Comment on the morphology of the red blood cells.
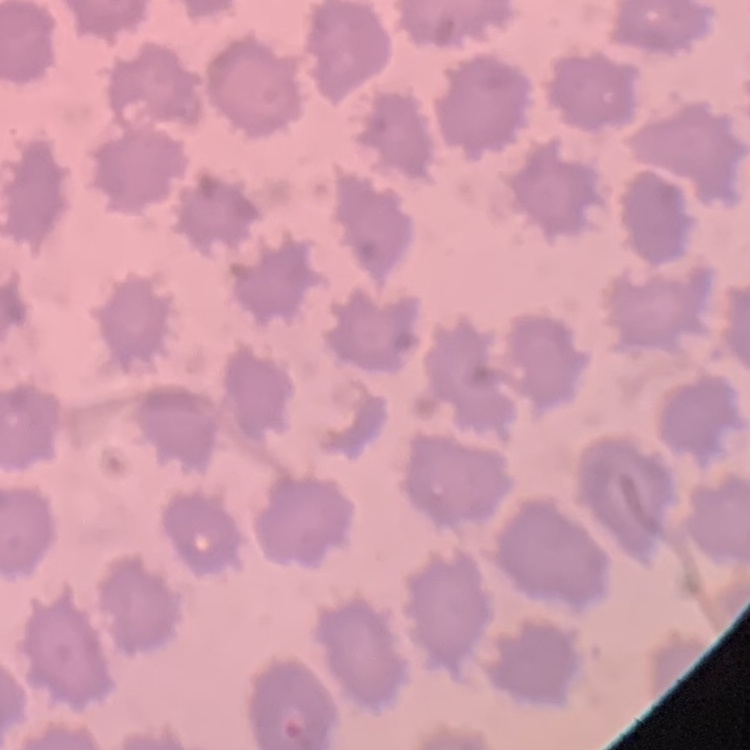
No rouleaux formation.

Field's or Giemsa stain. Thin blood smear. Square crop of a larger photomicrograph.